Identify the cell.
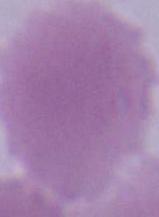
An erythrocyte.

modality = micrograph
magnification = 1000x